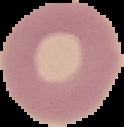

Summary:
  - Image type: segmented cell region with the area outside set to black
  - Image size: 124×127 pixels
  - Malaria status: uninfected
  - Preparation: thin blood smear